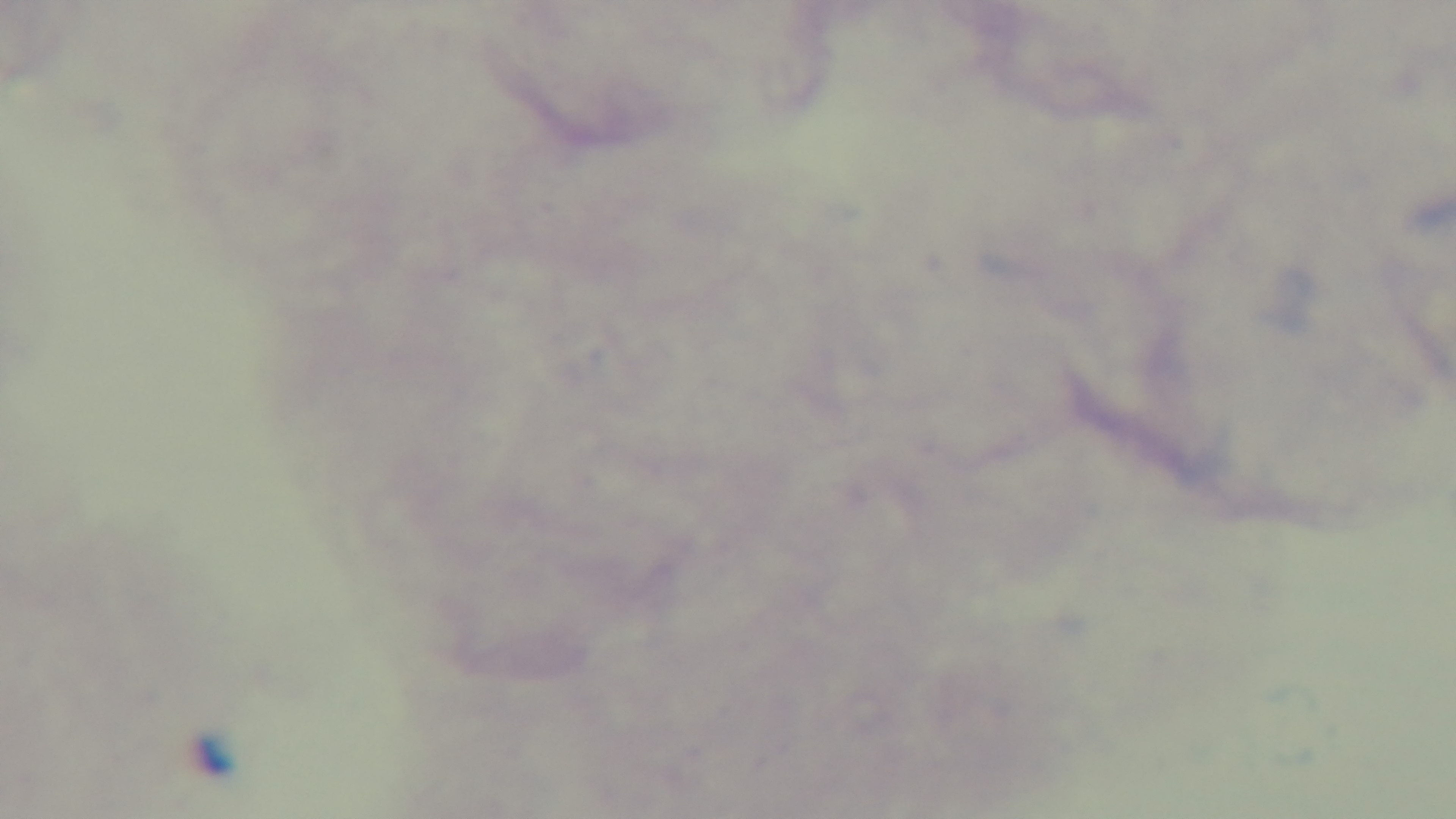
Summary:
  - Field of view: single
  - Modality: light microscopy
  - Malaria status: negative
  - Preparation: thick
  - Stain: Giemsa
  - Objective: 100x oil immersion
  - Capture: mounted 4K digital camera